Locate every blood parasite and identify its species.
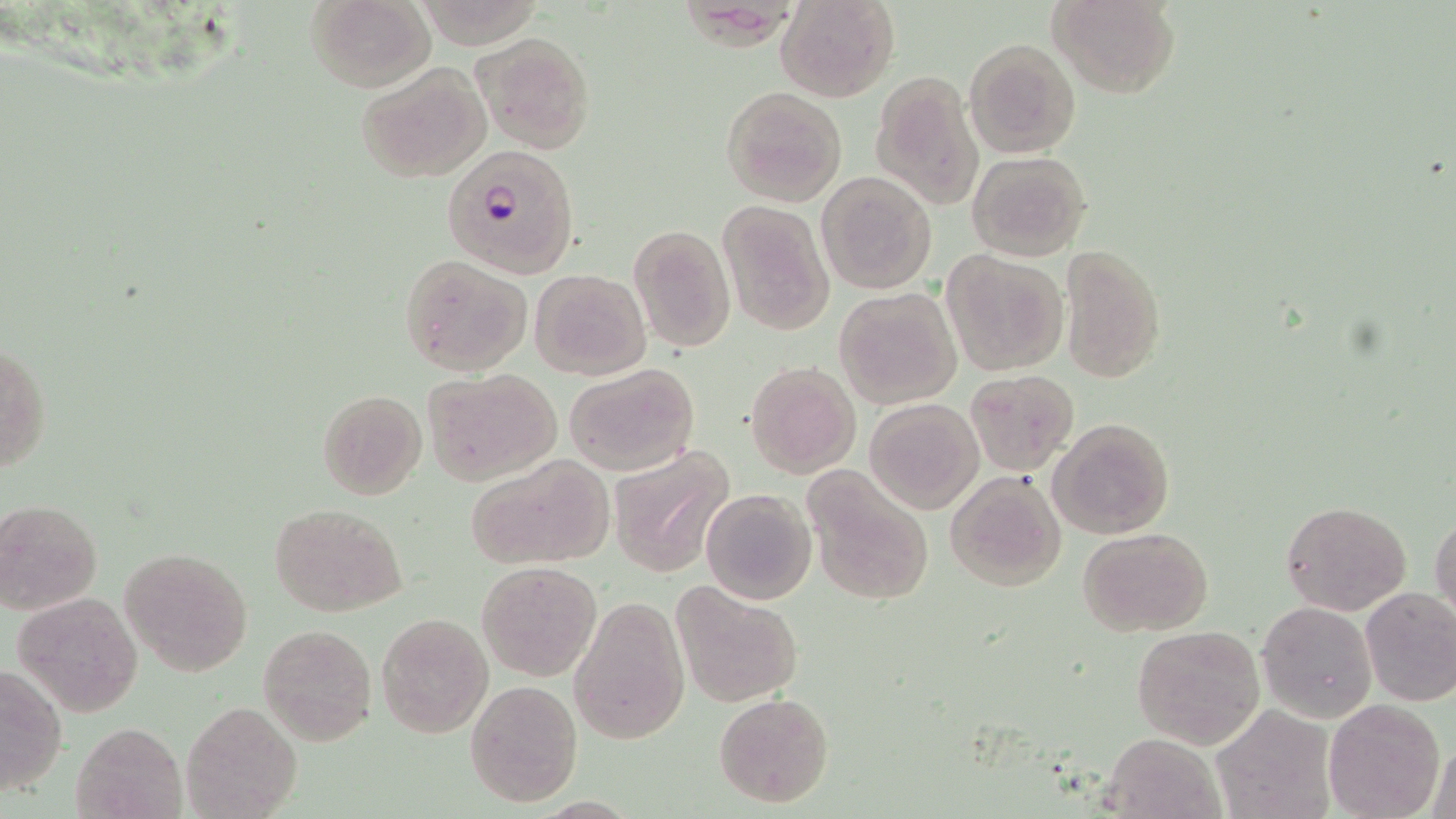
Approximate bounding boxes as (x1,y1)-(x2,y2) corner pairs in pixels.
Plasmodium falciparum-infected red blood cells: (441,144)-(580,277).
No Plasmodium ovale, Plasmodium malariae, Plasmodium vivax, Babesia divergens, or Trypanosoma brucei observed.

Uninfected red blood cell locations: (307,0)-(436,93), (778,0)-(898,102), (1051,0)-(1178,98), (474,32)-(595,152), (963,38)-(1082,158), (356,62)-(492,182), (871,71)-(984,211), (721,86)-(848,207), (965,149)-(1092,261), (816,171)-(939,295), (717,200)-(833,336), (629,224)-(736,353), (1059,245)-(1168,383), (943,251)-(1068,376), (397,254)-(531,377), (530,268)-(650,380), (834,288)-(960,409), (1,339)-(51,475), (746,361)-(861,478), (564,363)-(699,477), (421,368)-(559,485), (964,369)-(1078,475), (316,388)-(427,500), (865,397)-(983,514), (1049,416)-(1175,538), (610,445)-(735,578), (465,453)-(613,570), (802,470)-(935,606), (945,470)-(1067,591), (701,488)-(815,604), (0,499)-(103,613), (1280,499)-(1413,616), (268,502)-(407,617), (1431,513)-(1456,626), (1079,529)-(1212,638), (121,546)-(252,676), (475,562)-(602,681), (670,584)-(803,707), (1359,586)-(1456,706), (13,591)-(144,717), (570,598)-(689,745), (1256,601)-(1378,722), (375,611)-(492,738), (1131,623)-(1266,751), (259,624)-(378,746), (0,661)-(67,798), (466,680)-(582,806), (712,691)-(834,809), (181,699)-(305,818), (1323,700)-(1445,819), (1212,704)-(1336,819), (73,721)-(187,819), (1099,732)-(1226,819), (1425,737)-(1455,819). Slide-level diagnosis: Plasmodium falciparum. Thin blood smear. Light microscopy. Captured at 1000x magnification. May-Grünwald-Giemsa-stained preparation. One field of a larger specimen. Image is 1456×819 pixels.